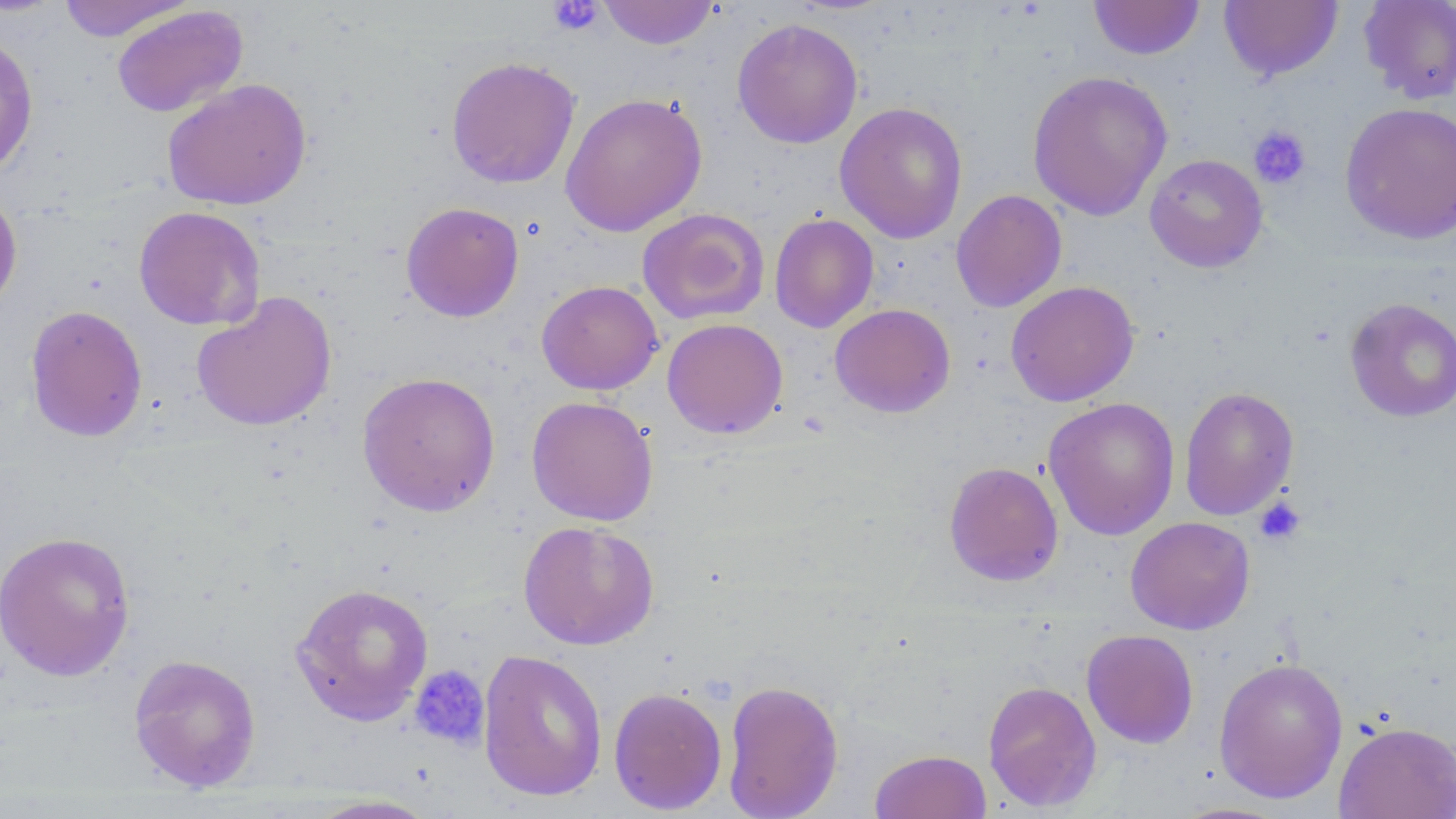 Approximate bounding boxes as named x1/y1/x2/y2 corners in pixels. Platelet locations: (x1=548, y1=0, x2=604, y2=36), (x1=1249, y1=125, x2=1311, y2=189), (x1=1254, y1=497, x2=1306, y2=545), (x1=408, y1=664, x2=491, y2=751). Uninfected red blood cell locations: (x1=56, y1=0, x2=195, y2=42), (x1=597, y1=0, x2=720, y2=50), (x1=1088, y1=0, x2=1205, y2=60), (x1=1358, y1=0, x2=1456, y2=105), (x1=1218, y1=1, x2=1343, y2=81), (x1=111, y1=5, x2=248, y2=117), (x1=732, y1=17, x2=863, y2=149), (x1=0, y1=32, x2=39, y2=179), (x1=445, y1=56, x2=581, y2=189), (x1=1026, y1=70, x2=1172, y2=221), (x1=163, y1=78, x2=312, y2=210), (x1=560, y1=92, x2=708, y2=237), (x1=834, y1=101, x2=968, y2=244), (x1=1339, y1=101, x2=1456, y2=245), (x1=1144, y1=153, x2=1268, y2=272), (x1=0, y1=185, x2=23, y2=317), (x1=950, y1=189, x2=1067, y2=313), (x1=401, y1=202, x2=525, y2=322), (x1=133, y1=206, x2=266, y2=330), (x1=636, y1=208, x2=771, y2=326), (x1=769, y1=213, x2=879, y2=333), (x1=536, y1=280, x2=663, y2=395), (x1=1005, y1=280, x2=1140, y2=407), (x1=191, y1=291, x2=338, y2=431), (x1=1344, y1=297, x2=1456, y2=422), (x1=829, y1=303, x2=956, y2=418), (x1=25, y1=304, x2=148, y2=443), (x1=662, y1=318, x2=788, y2=438), (x1=357, y1=371, x2=502, y2=517), (x1=1179, y1=386, x2=1299, y2=520), (x1=526, y1=395, x2=659, y2=526), (x1=1043, y1=396, x2=1180, y2=540), (x1=943, y1=461, x2=1064, y2=586), (x1=1125, y1=517, x2=1255, y2=635), (x1=518, y1=519, x2=659, y2=651), (x1=0, y1=530, x2=136, y2=681), (x1=290, y1=582, x2=434, y2=725), (x1=1081, y1=629, x2=1199, y2=748), (x1=477, y1=648, x2=608, y2=802), (x1=128, y1=653, x2=262, y2=792), (x1=1213, y1=657, x2=1348, y2=804), (x1=721, y1=679, x2=844, y2=819), (x1=982, y1=680, x2=1102, y2=811), (x1=608, y1=686, x2=728, y2=815), (x1=1334, y1=721, x2=1456, y2=818), (x1=869, y1=749, x2=992, y2=819), (x1=302, y1=794, x2=442, y2=818). Slide-level diagnosis: negative for blood parasites. May-Grünwald-Giemsa-stained preparation. One field of a larger specimen. Thin blood smear. Image is 1456×819 pixels. Optical microscopy. 1000x magnification.